Locate every blood parasite and identify its species.
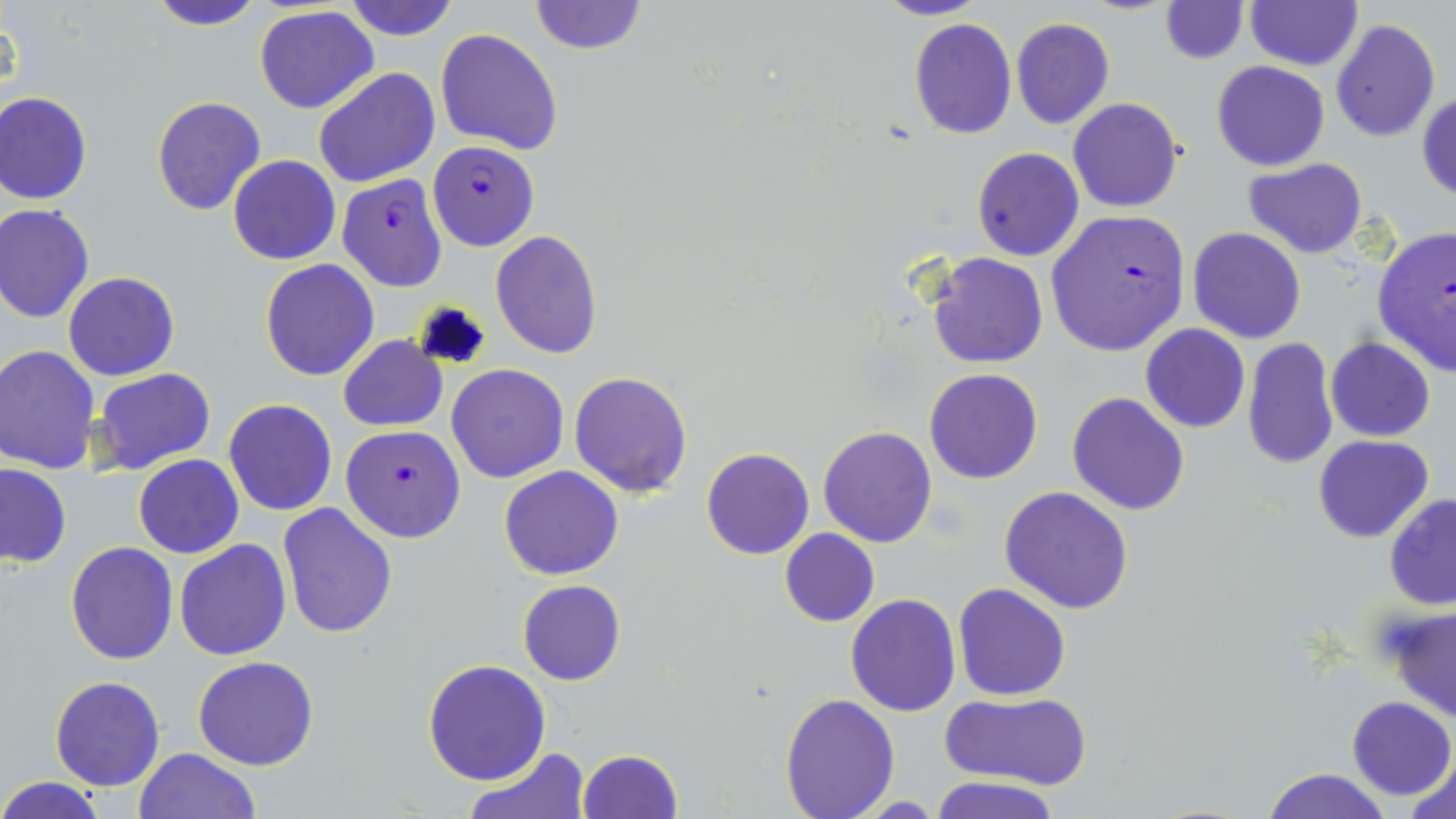

Approximate bounding boxes as (x1, y1, x2, y2) in pixels.
Plasmodium falciparum-infected red blood cells: (427, 141, 540, 250), (336, 175, 447, 292), (1045, 210, 1190, 357), (1372, 223, 1455, 376), (342, 424, 467, 543).
No Plasmodium ovale, Plasmodium malariae, Plasmodium vivax, Babesia divergens, or Trypanosoma brucei observed.

Uninfected red blood cell locations: (143, 0, 268, 32), (344, 0, 460, 40), (527, 0, 648, 56), (872, 0, 990, 21), (1159, 0, 1249, 63), (1245, 2, 1362, 71), (253, 6, 378, 112), (1012, 17, 1114, 130), (1330, 17, 1441, 143), (908, 19, 1017, 140), (435, 29, 563, 155), (1212, 61, 1329, 171), (313, 68, 439, 189), (0, 92, 93, 204), (1417, 92, 1456, 202), (152, 96, 267, 217), (1068, 99, 1182, 213), (972, 148, 1084, 261), (228, 154, 342, 265), (1243, 158, 1369, 257), (0, 204, 95, 322), (1187, 227, 1307, 344), (491, 229, 604, 359), (925, 250, 1049, 369), (260, 259, 380, 381), (65, 271, 179, 381), (1140, 324, 1250, 433), (338, 336, 447, 432), (1325, 336, 1436, 440), (1241, 337, 1339, 470), (0, 345, 101, 473), (445, 364, 568, 483), (92, 367, 216, 477), (924, 368, 1043, 485), (568, 371, 693, 496), (1066, 391, 1190, 514), (224, 398, 337, 515), (818, 424, 938, 546), (1312, 435, 1435, 543), (702, 447, 815, 559), (134, 455, 243, 558), (0, 463, 72, 567), (499, 465, 624, 580), (999, 486, 1133, 614), (1383, 493, 1456, 609), (278, 503, 398, 637), (780, 528, 879, 627), (174, 538, 291, 659), (65, 541, 179, 665), (518, 579, 624, 686), (954, 583, 1071, 700), (844, 594, 961, 716), (1387, 609, 1456, 726), (192, 657, 320, 771), (423, 660, 551, 785), (49, 676, 164, 791), (939, 690, 1093, 790), (779, 693, 900, 818), (1346, 696, 1454, 801), (465, 745, 586, 819), (134, 747, 257, 819), (576, 748, 683, 818), (1404, 759, 1456, 819), (1261, 767, 1391, 819), (933, 775, 1059, 819), (0, 777, 109, 818). Slide-level diagnosis: Plasmodium falciparum. Optical microscopy. Image is 1456×819 pixels. May-Grünwald-Giemsa stain. One field of a larger specimen. Captured at 1000x magnification. Thin blood smear.